Locate and identify every blood parasite.
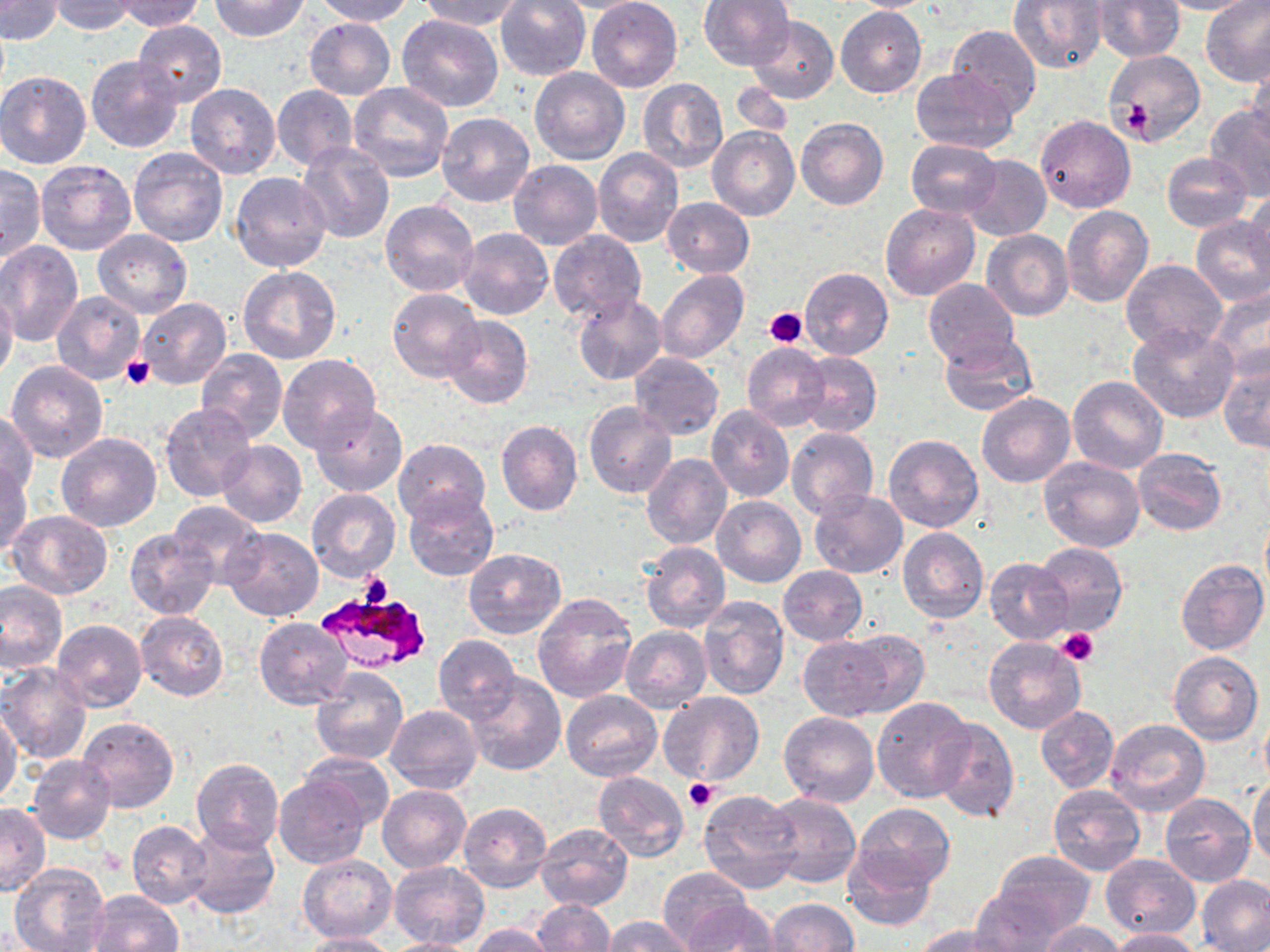

Approximate bounding boxes as [x1, y1, x2, y2] in pixels.
Plasmodium falciparum-infected red blood cells: [313, 587, 431, 673].
No Plasmodium ovale, Plasmodium malariae, Plasmodium vivax, Babesia divergens, or Trypanosoma brucei observed.

slide_level_diagnosis: Plasmodium falciparum
field_of_view: one of a larger specimen
preparation: thin blood smear
image_size: 1270×952 pixels
platelet_locations: 'approximate bounding boxes as [x1, y1, x2, y2] in pixels: [1124, 97, 1153, 137], [765, 308, 807, 348], [121, 356, 155, 390], [359, 573, 393, 607], [1057, 628, 1097, 665], [684, 777, 718, 812]'
modality: optical microscopy
stain: May-Grünwald-Giemsa
magnification: 1000x
uninfected_red_blood_cell_locations: 'approximate bounding boxes as [x1, y1, x2, y2] in pixels: [0, 0, 63, 43], [114, 0, 206, 31], [208, 0, 310, 41], [312, 0, 412, 25], [418, 0, 522, 31], [586, 0, 682, 92], [1010, 0, 1108, 72], [1092, 0, 1184, 62], [1154, 0, 1260, 15], [1199, 0, 1270, 87], [50, 1, 140, 34], [496, 1, 590, 80], [698, 1, 796, 72], [844, 1, 942, 12], [836, 7, 927, 98], [397, 14, 504, 113], [746, 16, 838, 105], [304, 18, 395, 100], [132, 21, 226, 108], [946, 25, 1042, 116], [152, 30, 248, 149], [1104, 49, 1204, 145], [86, 56, 182, 154], [1247, 59, 1270, 150], [530, 68, 630, 164], [911, 68, 1017, 152], [0, 71, 90, 169], [637, 78, 728, 173], [729, 82, 794, 139], [185, 84, 282, 180], [348, 84, 455, 182], [273, 85, 358, 171], [1205, 104, 1270, 199], [437, 113, 535, 208], [1035, 114, 1135, 214], [796, 118, 888, 209], [708, 125, 800, 221], [905, 139, 1001, 219], [297, 142, 395, 245], [129, 148, 228, 247], [593, 149, 684, 247], [1161, 153, 1252, 232], [961, 154, 1051, 241], [36, 160, 136, 256], [508, 160, 602, 250], [0, 164, 45, 262], [230, 172, 331, 274], [1246, 187, 1270, 276], [662, 197, 754, 277], [381, 200, 480, 298], [881, 202, 979, 300], [1061, 207, 1154, 309], [1191, 216, 1270, 307], [457, 227, 553, 321], [92, 229, 193, 318], [548, 230, 646, 324], [982, 230, 1073, 320], [0, 240, 82, 345], [1121, 259, 1227, 355], [238, 265, 341, 364], [800, 267, 893, 360], [656, 270, 748, 362], [923, 279, 1021, 368], [1208, 286, 1270, 384], [0, 287, 18, 382], [388, 289, 483, 383], [52, 290, 146, 385], [573, 294, 667, 386], [135, 298, 233, 390], [441, 314, 531, 409], [1127, 323, 1240, 423], [937, 333, 1039, 418], [742, 343, 829, 430], [194, 348, 288, 443], [1218, 350, 1270, 456], [797, 351, 881, 438], [629, 352, 724, 440], [276, 355, 381, 455], [6, 360, 109, 462], [1069, 375, 1166, 473], [977, 393, 1075, 487], [584, 402, 676, 499], [159, 404, 259, 503], [311, 404, 406, 495], [706, 406, 794, 502], [1, 409, 38, 498], [712, 414, 877, 505], [496, 420, 583, 516], [787, 427, 878, 520], [55, 432, 161, 531], [883, 434, 982, 532], [392, 438, 489, 527], [215, 439, 306, 527], [1132, 448, 1226, 536], [642, 452, 733, 550], [1038, 456, 1145, 553], [0, 460, 32, 556], [307, 489, 400, 581], [809, 490, 907, 579], [404, 492, 497, 580], [712, 497, 806, 588], [168, 501, 265, 583], [7, 510, 113, 598], [222, 527, 323, 621], [898, 528, 988, 625], [125, 529, 218, 620], [641, 542, 730, 633], [1033, 543, 1127, 636], [463, 548, 566, 637], [985, 558, 1072, 643], [1176, 558, 1269, 655], [778, 566, 867, 646], [0, 578, 67, 672], [534, 594, 637, 703], [698, 596, 789, 699], [136, 611, 229, 701], [254, 617, 355, 710], [53, 619, 146, 710], [620, 626, 710, 712], [798, 635, 904, 721], [434, 636, 520, 721], [983, 637, 1086, 733], [1169, 650, 1263, 745], [0, 664, 91, 765], [310, 669, 408, 766], [464, 672, 565, 774], [562, 690, 662, 782], [660, 690, 763, 786], [871, 697, 977, 802], [1258, 702, 1269, 793], [386, 705, 482, 794], [1035, 706, 1118, 792], [0, 709, 21, 807], [780, 711, 879, 806], [78, 716, 178, 813], [931, 717, 1020, 824], [1104, 719, 1209, 817], [299, 751, 396, 831], [27, 755, 116, 844], [192, 758, 283, 853], [593, 771, 689, 861], [274, 774, 369, 869], [1247, 775, 1270, 868], [1048, 784, 1147, 876], [378, 786, 470, 872], [698, 789, 802, 893], [764, 793, 860, 889], [1160, 793, 1255, 886], [457, 802, 551, 893], [851, 802, 953, 892], [1, 803, 49, 895], [127, 821, 212, 909], [183, 823, 279, 919], [534, 823, 632, 911], [842, 845, 939, 932], [989, 849, 1097, 941], [1100, 853, 1200, 940], [297, 854, 396, 943], [388, 861, 489, 950], [9, 864, 110, 952], [658, 868, 751, 950], [1197, 874, 1270, 951], [972, 884, 1073, 952], [89, 891, 184, 952], [531, 899, 615, 951], [765, 899, 859, 951], [681, 900, 782, 951], [602, 916, 695, 952], [1037, 922, 1125, 952], [469, 925, 559, 952], [913, 925, 1018, 951], [1106, 928, 1202, 951], [295, 932, 399, 951], [378, 937, 485, 952]'